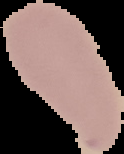
Summary:
  - Preparation: thin blood film
  - Result: no malaria parasites detected
  - Image size: 124×154 pixels
  - Image type: segmented cell region with the area outside set to black